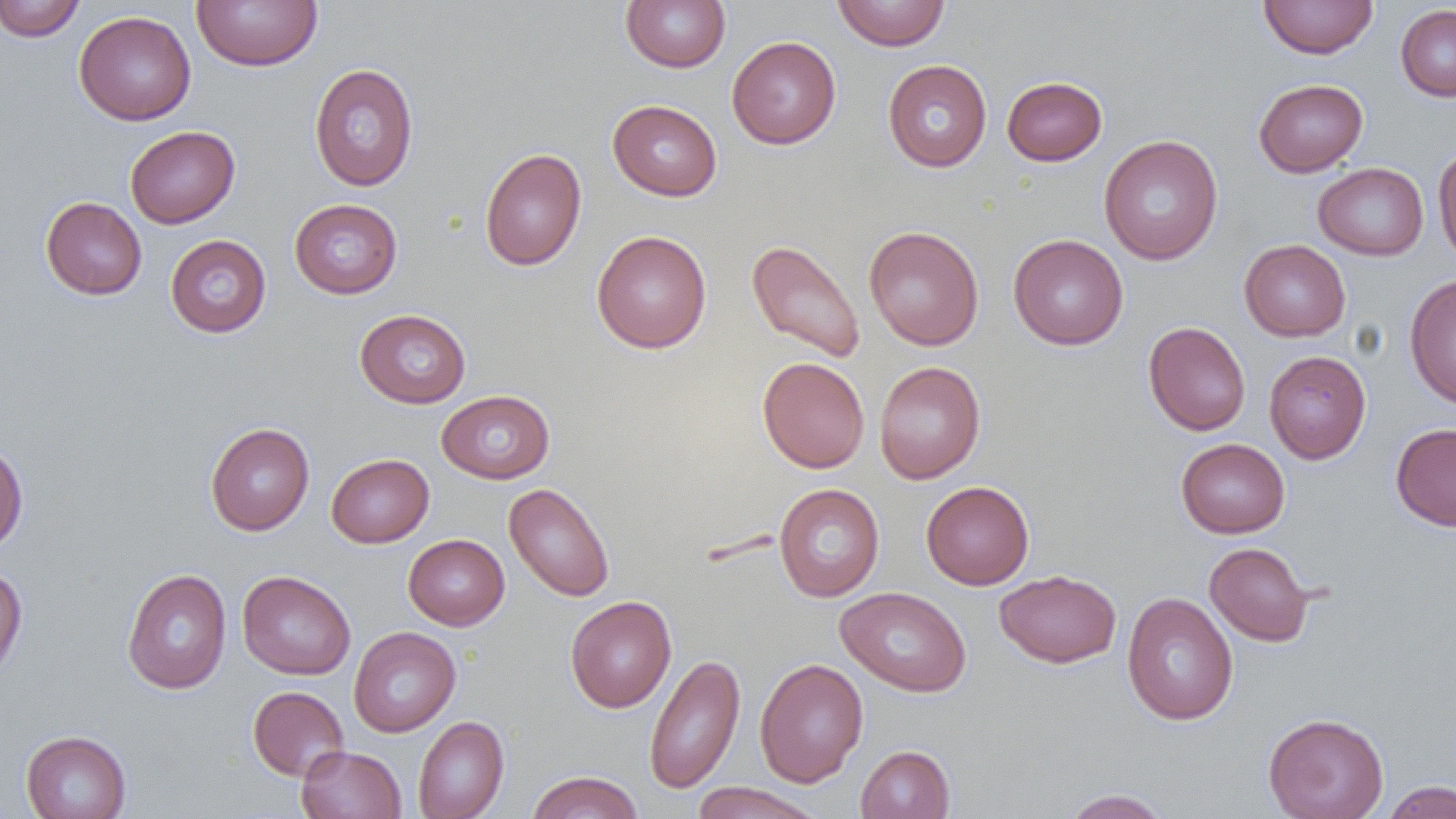

Approximate bounding boxes as (x1,y1)-(x2,y2) corner pairs in pixels. Uninfected red blood cell locations: (1,0)-(87,42), (191,0)-(323,71), (620,0)-(731,72), (832,0)-(950,51), (1259,0)-(1378,59), (1396,4)-(1456,102), (74,10)-(197,125), (727,36)-(841,149), (882,59)-(992,172), (308,63)-(419,191), (1002,76)-(1107,165), (1254,79)-(1368,177), (607,99)-(722,201), (125,126)-(239,228), (1098,135)-(1223,265), (1433,143)-(1456,270), (479,148)-(587,271), (1313,163)-(1429,260), (40,196)-(147,300), (289,198)-(402,298), (863,225)-(984,350), (592,230)-(712,354), (1008,233)-(1128,351), (165,234)-(272,337), (747,239)-(865,363), (1239,239)-(1351,341), (1404,273)-(1456,409), (354,309)-(471,408), (1143,321)-(1251,436), (1264,350)-(1371,463), (757,356)-(869,473), (874,360)-(986,484), (437,389)-(555,484), (205,423)-(314,535), (1390,423)-(1456,532), (1176,438)-(1290,538), (0,442)-(28,553), (326,453)-(434,547), (921,480)-(1034,589), (504,483)-(615,602), (774,483)-(885,601), (403,534)-(510,630), (1204,542)-(1315,647), (0,564)-(28,681), (121,569)-(232,695), (994,569)-(1122,668), (237,570)-(356,679), (836,586)-(973,697), (1121,591)-(1238,726), (565,595)-(677,713), (348,627)-(461,737), (644,652)-(746,794), (754,658)-(869,787), (248,685)-(349,781), (1263,712)-(1389,819), (413,716)-(509,819), (21,730)-(132,819), (296,744)-(406,819), (855,744)-(955,819), (526,770)-(644,819), (1381,780)-(1456,819), (690,782)-(825,819), (1060,789)-(1172,818). Slide-level diagnosis: no evidence of blood parasites. Optical microscopy. Image is 1456×819 pixels. Thin blood film. 1000x magnification. One field of a larger specimen.